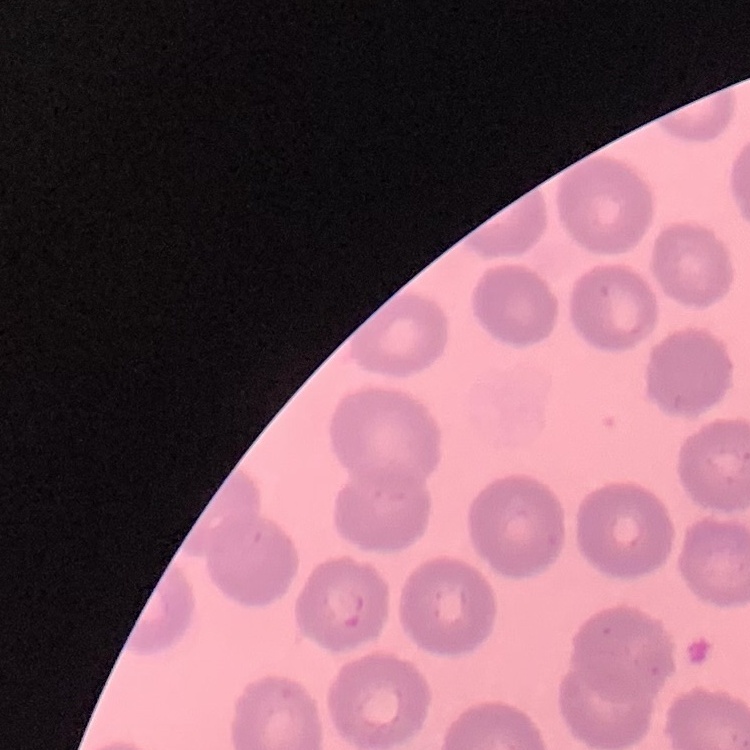

The erythrocytes show no rouleaux formation. Thin blood film. One tile cut from a larger photomicrograph. Stained with either Field's or Giemsa.